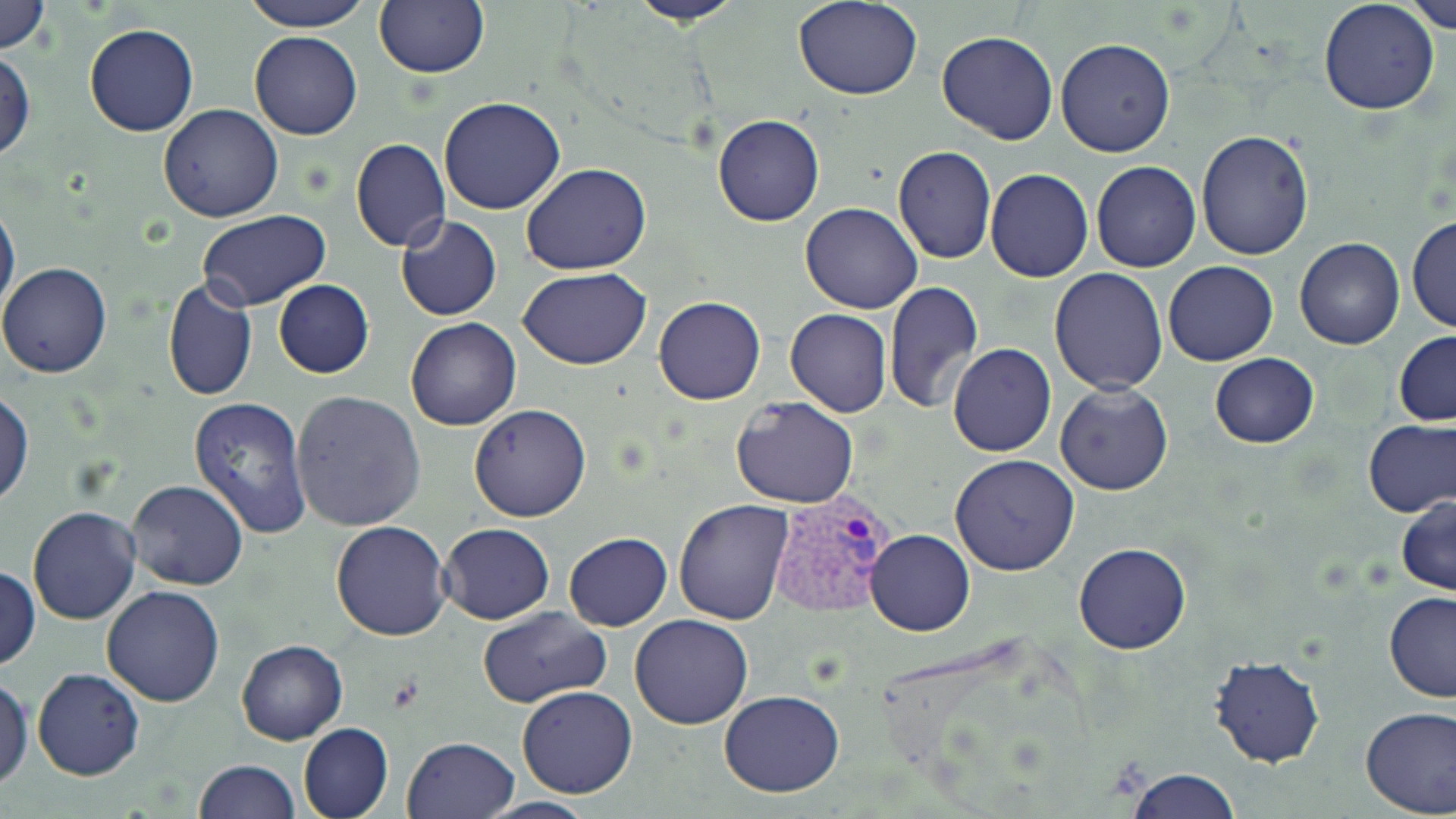
Approximate bounding boxes as [x1, y1, x2, y2] in pixels. Uninfected red blood cell locations: [0, 0, 50, 55], [238, 0, 374, 32], [374, 0, 488, 79], [629, 0, 748, 27], [794, 0, 924, 100], [1406, 0, 1456, 33], [1318, 2, 1440, 115], [84, 23, 198, 137], [250, 30, 362, 140], [936, 30, 1057, 145], [1056, 37, 1174, 158], [0, 50, 36, 162], [438, 97, 565, 215], [158, 104, 284, 222], [712, 113, 824, 225], [1195, 130, 1316, 261], [350, 137, 450, 251], [892, 146, 996, 263], [1092, 161, 1201, 273], [521, 163, 652, 276], [985, 168, 1094, 283], [0, 197, 20, 325], [799, 202, 924, 313], [199, 210, 331, 310], [394, 216, 503, 322], [1407, 217, 1456, 335], [1295, 239, 1405, 350], [1163, 261, 1278, 366], [0, 262, 112, 379], [518, 267, 652, 368], [1048, 267, 1169, 394], [162, 279, 257, 404], [273, 280, 374, 379], [883, 281, 984, 415], [654, 295, 766, 405], [786, 309, 892, 418], [406, 317, 521, 432], [1394, 330, 1456, 427], [948, 343, 1056, 458], [1209, 352, 1320, 449], [1055, 382, 1174, 496], [292, 390, 426, 532], [0, 391, 34, 507], [730, 395, 859, 508], [188, 396, 313, 539], [469, 403, 591, 522], [1363, 417, 1455, 518], [949, 454, 1078, 576], [128, 481, 248, 590], [1396, 495, 1456, 595], [674, 497, 793, 623], [27, 505, 140, 624], [330, 520, 452, 641], [438, 523, 554, 624], [865, 529, 975, 636], [564, 533, 671, 631], [1074, 541, 1191, 655], [0, 563, 40, 670], [102, 585, 225, 708], [1383, 591, 1456, 703], [476, 606, 612, 710], [629, 614, 754, 729], [236, 639, 348, 745], [1210, 655, 1325, 768], [32, 668, 145, 779], [0, 671, 33, 791], [516, 684, 638, 798], [719, 690, 845, 797], [1359, 705, 1456, 818], [298, 723, 394, 819], [402, 736, 519, 818], [194, 759, 300, 818], [1124, 767, 1240, 819], [474, 796, 597, 818]. Plasmodium vivax-infected red blood cell locations: [766, 488, 896, 623]. Slide-level diagnosis: Plasmodium vivax. Captured at 1000x magnification. May-Grünwald-Giemsa stain. One field of a larger specimen. Thin blood film. Optical microscopy. Image is 1456×819 pixels.